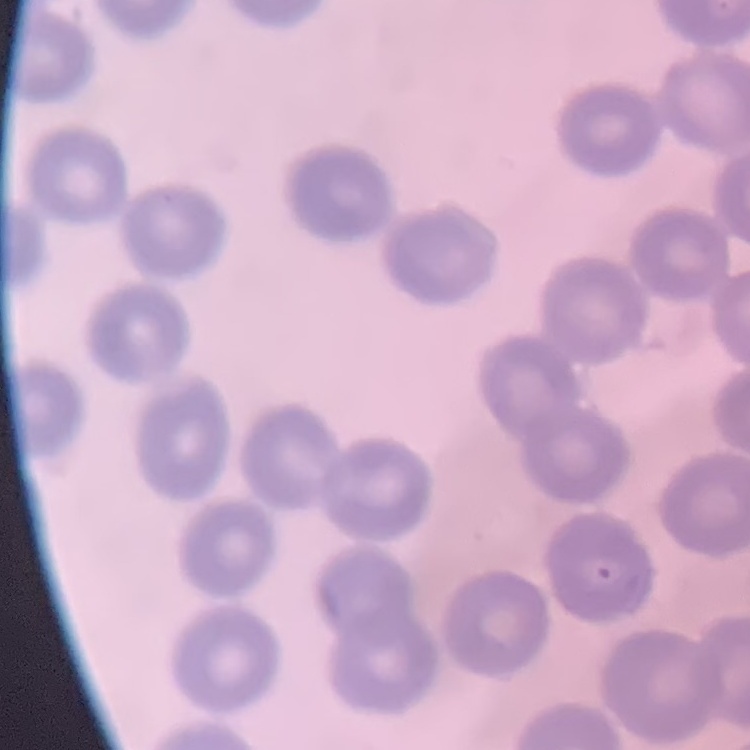
Summary:
  - Red blood cell morphology: no rouleaux formation
  - Image type: square crop of a larger photomicrograph
  - Stain: Field's or Giemsa
  - Preparation: thin blood film